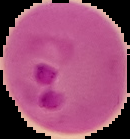

{
  "image_size": "130×139 pixels",
  "preparation": "thin blood smear",
  "image_type": "segmented cell region with the area outside set to black",
  "result": "malaria parasites detected"
}